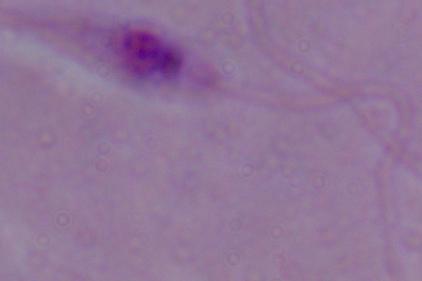 Micrograph. Captured at 1000x magnification. A Leishmania parasite is seen.